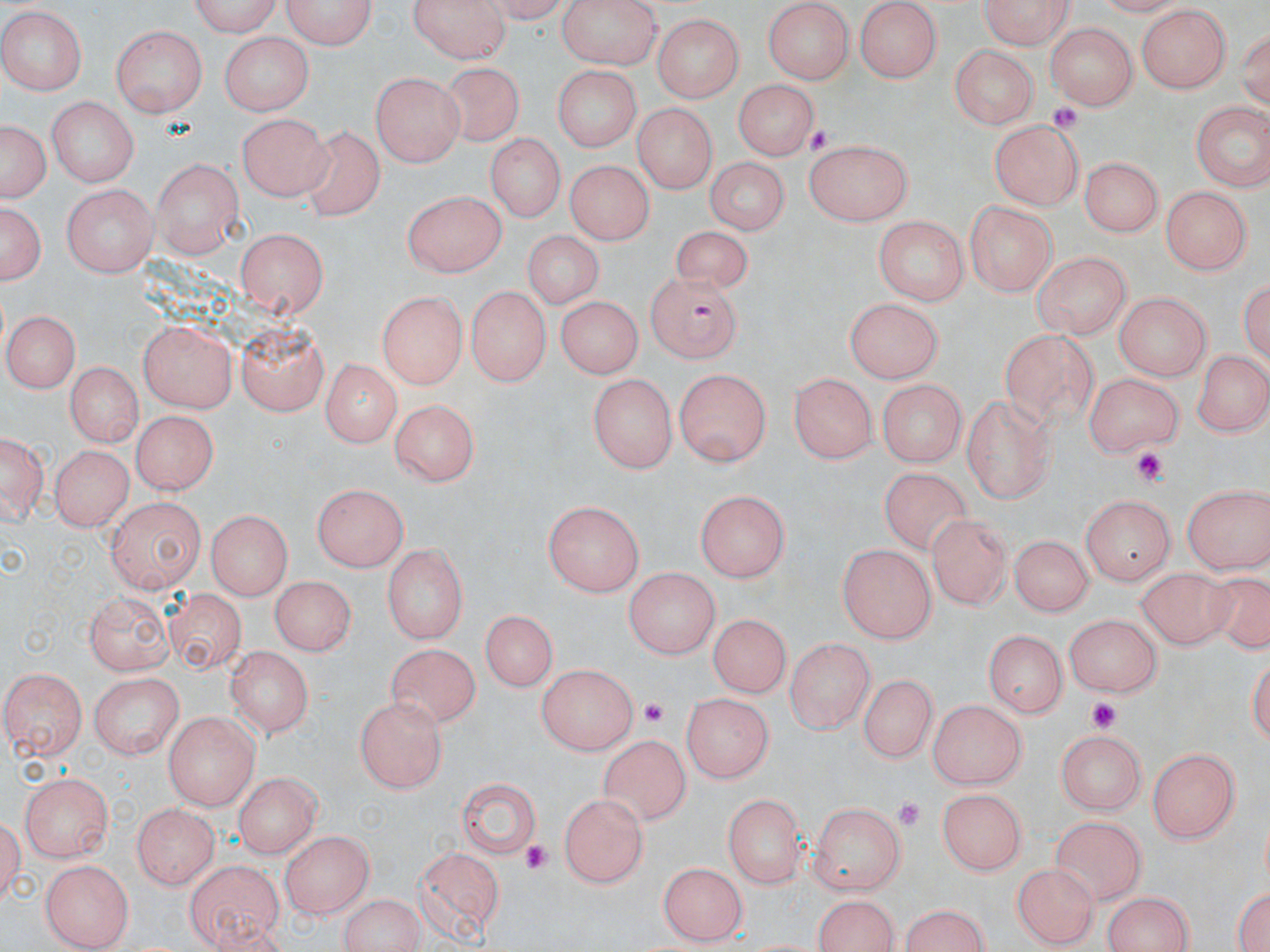

Summary:
  - Coordinate format: approximate bounding boxes as (x1,y1)-(x2,y2) corner pairs in pixels
  - Uninfected red blood cell locations: (179,0)-(283,36), (282,0)-(374,49), (410,0)-(510,64), (555,0)-(659,69), (856,0)-(940,81), (977,0)-(1076,44), (764,3)-(851,82), (1133,6)-(1229,94), (0,9)-(85,95), (652,11)-(748,105), (1044,24)-(1133,110), (110,25)-(208,119), (221,33)-(311,114), (948,44)-(1036,130), (442,63)-(527,151), (549,65)-(644,153), (370,73)-(465,168), (734,78)-(823,158), (47,98)-(140,186), (1189,100)-(1267,189), (630,103)-(715,193), (236,112)-(332,200), (2,117)-(47,203), (990,119)-(1083,209), (298,125)-(390,225), (487,133)-(566,227), (804,137)-(914,227), (1081,156)-(1162,240), (151,157)-(240,255), (567,159)-(652,246), (702,159)-(786,234), (63,184)-(156,278), (1161,186)-(1251,275), (402,190)-(504,278), (1,199)-(46,292), (964,199)-(1057,296), (869,217)-(969,306), (234,226)-(327,320), (676,226)-(751,294), (519,229)-(607,308), (1033,251)-(1130,339), (1239,269)-(1270,367), (466,284)-(554,386), (376,292)-(466,390), (1111,292)-(1213,377), (553,295)-(643,380), (841,297)-(943,383), (5,308)-(81,392), (137,321)-(237,413), (234,322)-(330,417), (993,323)-(1106,439), (1193,347)-(1269,438), (63,360)-(139,448), (319,360)-(400,446), (673,367)-(771,468), (1081,372)-(1184,453), (588,374)-(678,473), (788,374)-(876,465), (877,378)-(966,465), (962,393)-(1055,501), (390,397)-(481,485), (132,413)-(214,494), (2,429)-(47,526), (50,444)-(132,533), (876,460)-(979,557), (310,483)-(407,572), (1182,483)-(1270,573), (694,491)-(794,583), (1082,493)-(1176,585), (106,495)-(203,593), (543,500)-(644,598), (203,510)-(292,600), (930,514)-(1011,606), (1007,535)-(1094,615), (836,543)-(937,643), (381,545)-(466,643), (1134,566)-(1225,650), (624,569)-(718,661), (1201,569)-(1270,660), (269,573)-(351,656), (82,590)-(175,676), (172,599)-(243,673), (479,612)-(557,692), (1065,612)-(1165,697), (706,613)-(791,700), (983,629)-(1064,719), (783,640)-(874,732), (386,642)-(479,728), (226,648)-(312,738), (536,663)-(640,757), (3,668)-(88,760), (86,670)-(186,756), (855,672)-(933,765), (680,689)-(771,784), (355,698)-(447,793), (928,698)-(1026,789), (163,709)-(261,807), (1057,727)-(1145,814), (596,734)-(690,822), (1149,745)-(1244,842), (233,769)-(319,859), (18,770)-(118,863), (456,776)-(544,865), (934,791)-(1025,879), (558,792)-(650,886), (722,793)-(805,887), (808,801)-(905,895), (132,803)-(221,890), (1046,817)-(1146,903), (278,832)-(372,918), (415,842)-(507,941), (38,857)-(135,947), (184,860)-(284,950), (659,863)-(751,945), (1011,863)-(1097,947), (1231,879)-(1270,952), (336,891)-(427,951), (1100,891)-(1199,951), (810,892)-(904,951), (899,904)-(994,952)
  - Plasmodium falciparum-infected red blood cell locations: (643,271)-(747,361)
  - Platelet locations: (1044,103)-(1085,135), (1129,447)-(1170,490), (638,696)-(669,725), (1078,697)-(1125,734), (889,796)-(926,830), (521,841)-(552,875)
  - Slide-level diagnosis: Plasmodium falciparum
  - Preparation: thin blood smear
  - Stain: May-Grünwald-Giemsa
  - Modality: light microscopy
  - Field of view: single
  - Image size: 1270×952 pixels
  - Magnification: 1000x